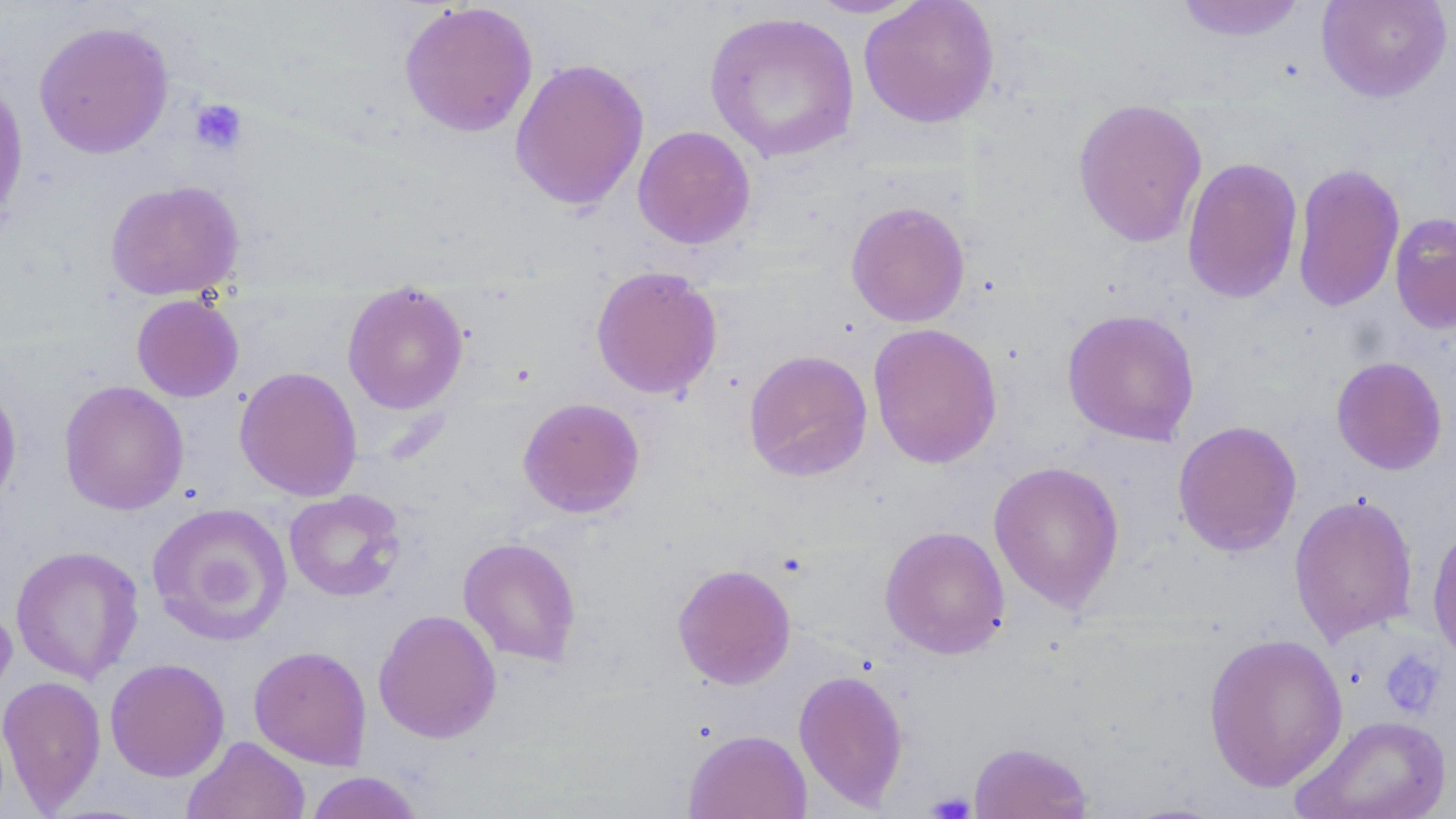

Summary:
  - Coordinate format: approximate bounding boxes as (x1,y1)-(x2,y2) corner pairs in pixels
  - Platelet locations: (190,99)-(248,155), (1378,648)-(1446,718), (927,791)-(976,819)
  - Uninfected red blood cell locations: (804,0)-(926,19), (858,0)-(999,128), (1172,0)-(1309,43), (1316,0)-(1453,102), (398,2)-(539,137), (704,10)-(860,164), (33,20)-(175,159), (509,58)-(650,211), (0,72)-(30,230), (1072,97)-(1209,248), (632,125)-(756,250), (1182,156)-(1303,304), (1291,161)-(1405,313), (105,179)-(244,300), (846,200)-(970,327), (1389,213)-(1456,335), (590,265)-(722,400), (341,282)-(470,415), (131,294)-(244,402), (1061,308)-(1200,446), (867,322)-(1003,470), (743,349)-(872,482), (1331,356)-(1448,475), (234,366)-(363,501), (0,379)-(23,513), (59,380)-(189,516), (517,397)-(645,518), (1172,420)-(1302,557), (988,460)-(1125,613), (284,489)-(406,602), (1288,492)-(1419,645), (146,502)-(292,646), (1427,522)-(1456,665), (879,525)-(1010,659), (458,537)-(582,666), (10,545)-(144,684), (672,563)-(797,689), (0,601)-(17,704), (373,609)-(502,744), (1202,632)-(1349,792), (248,645)-(372,769), (105,658)-(230,782), (792,668)-(910,810), (0,674)-(106,813), (1292,714)-(1453,819), (683,728)-(811,818), (183,736)-(311,819), (968,741)-(1093,818), (304,771)-(425,818)
  - Slide-level diagnosis: no evidence of blood parasites
  - Image size: 1456×819 pixels
  - Preparation: thin blood film
  - Modality: optical microscopy
  - Stain: May-Grünwald-Giemsa
  - Field of view: single
  - Magnification: 1000x